State which parasite is depicted.
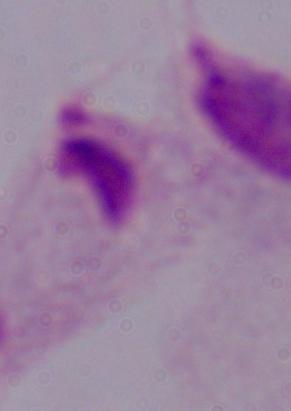
A trichomonad.

Summary:
  - Magnification: 1000x
  - Modality: photomicrograph